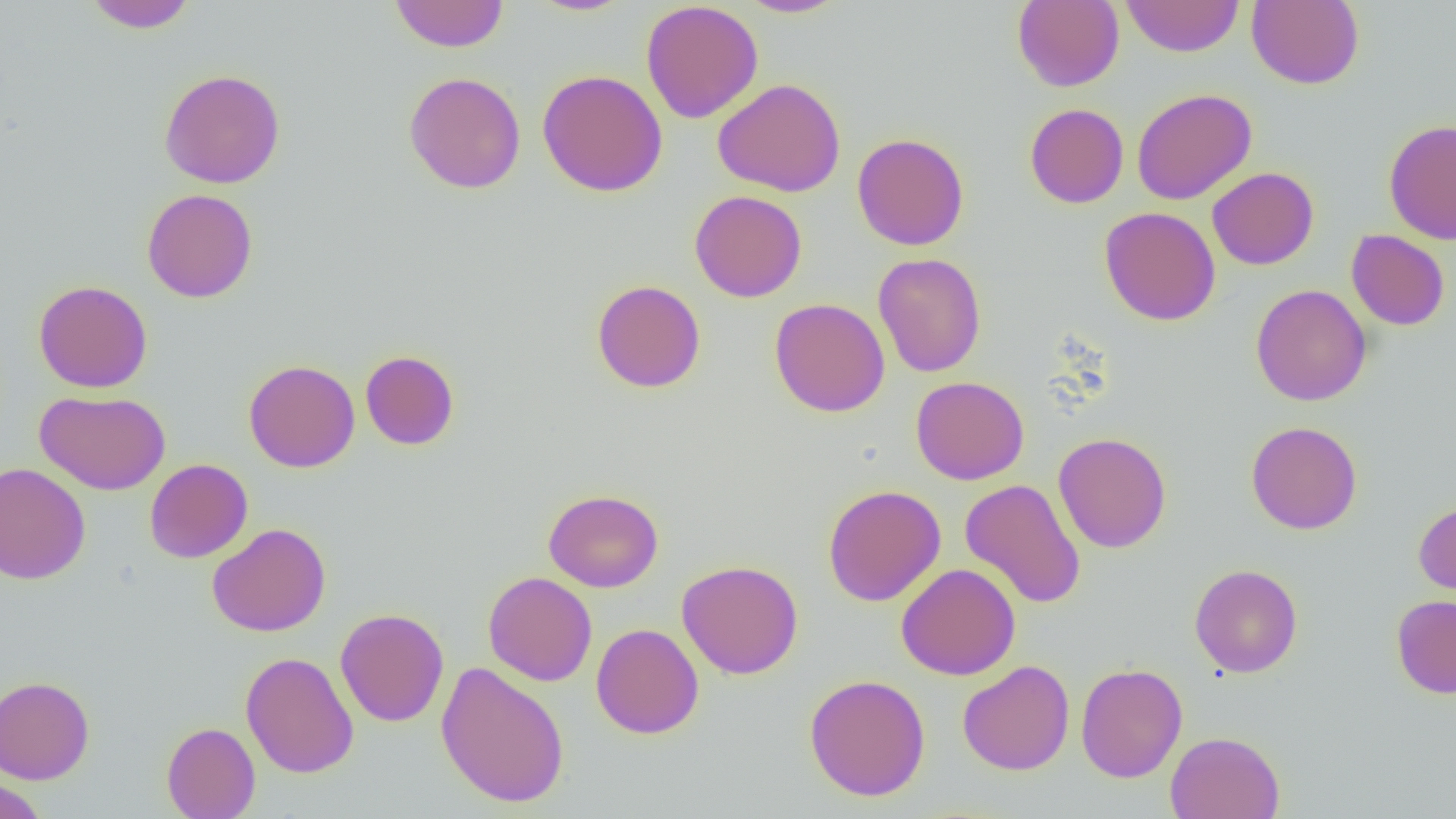
Summary:
  - Coordinate format: approximate bounding boxes as named x1/y1/x2/y2 corners in pixels
  - Uninfected red blood cell locations: (x1=83, y1=0, x2=198, y2=33), (x1=527, y1=0, x2=635, y2=16), (x1=737, y1=0, x2=849, y2=18), (x1=1012, y1=0, x2=1124, y2=92), (x1=1121, y1=0, x2=1244, y2=57), (x1=1246, y1=0, x2=1364, y2=89), (x1=389, y1=1, x2=509, y2=52), (x1=640, y1=1, x2=764, y2=123), (x1=158, y1=68, x2=286, y2=189), (x1=537, y1=69, x2=668, y2=197), (x1=403, y1=71, x2=526, y2=194), (x1=713, y1=78, x2=846, y2=197), (x1=1132, y1=88, x2=1258, y2=205), (x1=1024, y1=103, x2=1129, y2=208), (x1=1384, y1=119, x2=1456, y2=244), (x1=852, y1=133, x2=969, y2=250), (x1=1207, y1=167, x2=1319, y2=270), (x1=142, y1=188, x2=258, y2=303), (x1=689, y1=190, x2=807, y2=302), (x1=1099, y1=207, x2=1221, y2=326), (x1=1346, y1=229, x2=1450, y2=330), (x1=873, y1=253, x2=986, y2=378), (x1=33, y1=280, x2=153, y2=393), (x1=592, y1=280, x2=706, y2=393), (x1=1250, y1=284, x2=1372, y2=406), (x1=769, y1=298, x2=890, y2=417), (x1=360, y1=350, x2=460, y2=450), (x1=243, y1=359, x2=360, y2=473), (x1=910, y1=376, x2=1029, y2=484), (x1=35, y1=390, x2=171, y2=495), (x1=1247, y1=420, x2=1363, y2=535), (x1=1052, y1=432, x2=1171, y2=553), (x1=144, y1=458, x2=253, y2=563), (x1=0, y1=462, x2=91, y2=585), (x1=960, y1=478, x2=1086, y2=609), (x1=822, y1=485, x2=946, y2=606), (x1=543, y1=488, x2=664, y2=592), (x1=1413, y1=500, x2=1456, y2=602), (x1=207, y1=522, x2=331, y2=637), (x1=676, y1=559, x2=804, y2=680), (x1=896, y1=563, x2=1021, y2=680), (x1=1189, y1=563, x2=1303, y2=678), (x1=483, y1=571, x2=597, y2=686), (x1=1391, y1=594, x2=1456, y2=699), (x1=335, y1=607, x2=449, y2=727), (x1=591, y1=623, x2=704, y2=739), (x1=240, y1=650, x2=358, y2=779), (x1=958, y1=660, x2=1075, y2=776), (x1=435, y1=661, x2=571, y2=808), (x1=1075, y1=663, x2=1187, y2=783), (x1=804, y1=674, x2=931, y2=801), (x1=0, y1=676, x2=95, y2=784), (x1=162, y1=722, x2=260, y2=819), (x1=1165, y1=731, x2=1285, y2=819), (x1=0, y1=775, x2=48, y2=819)
  - Slide-level diagnosis: negative for blood parasites
  - Image size: 1456×819 pixels
  - Magnification: 1000x
  - Preparation: thin blood smear
  - Field of view: one of a larger specimen
  - Modality: light microscopy